Classify this cell by malaria status.
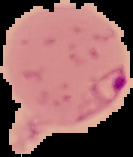
It is parasitized.

Summary:
  - Image size: 133×157 pixels
  - Image type: segmented cell region with the area outside set to black
  - Preparation: thin blood film